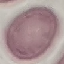
Summary:
  - Result: negative for malaria parasites
  - Capture: smartphone through the microscope eyepiece
  - Preparation: thin blood film
  - Stain: Giemsa
  - Image type: cell patch, automatically extracted from a larger field of view and resized to 64 × 64 pixels